Report the malaria status of this cell.
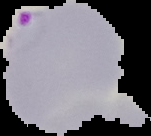
It is parasitized.

image size = 151×136 pixels
image type = cell region segmented out of the field of view; surrounding area masked to black
preparation = thin blood film